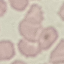
Summary:
  - Result: no malaria parasites detected
  - Capture: smartphone through the microscope eyepiece
  - Preparation: thin blood film
  - Stain: Giemsa
  - Image type: cell patch, automatically extracted from a larger field of view and resized to 64 × 64 pixels